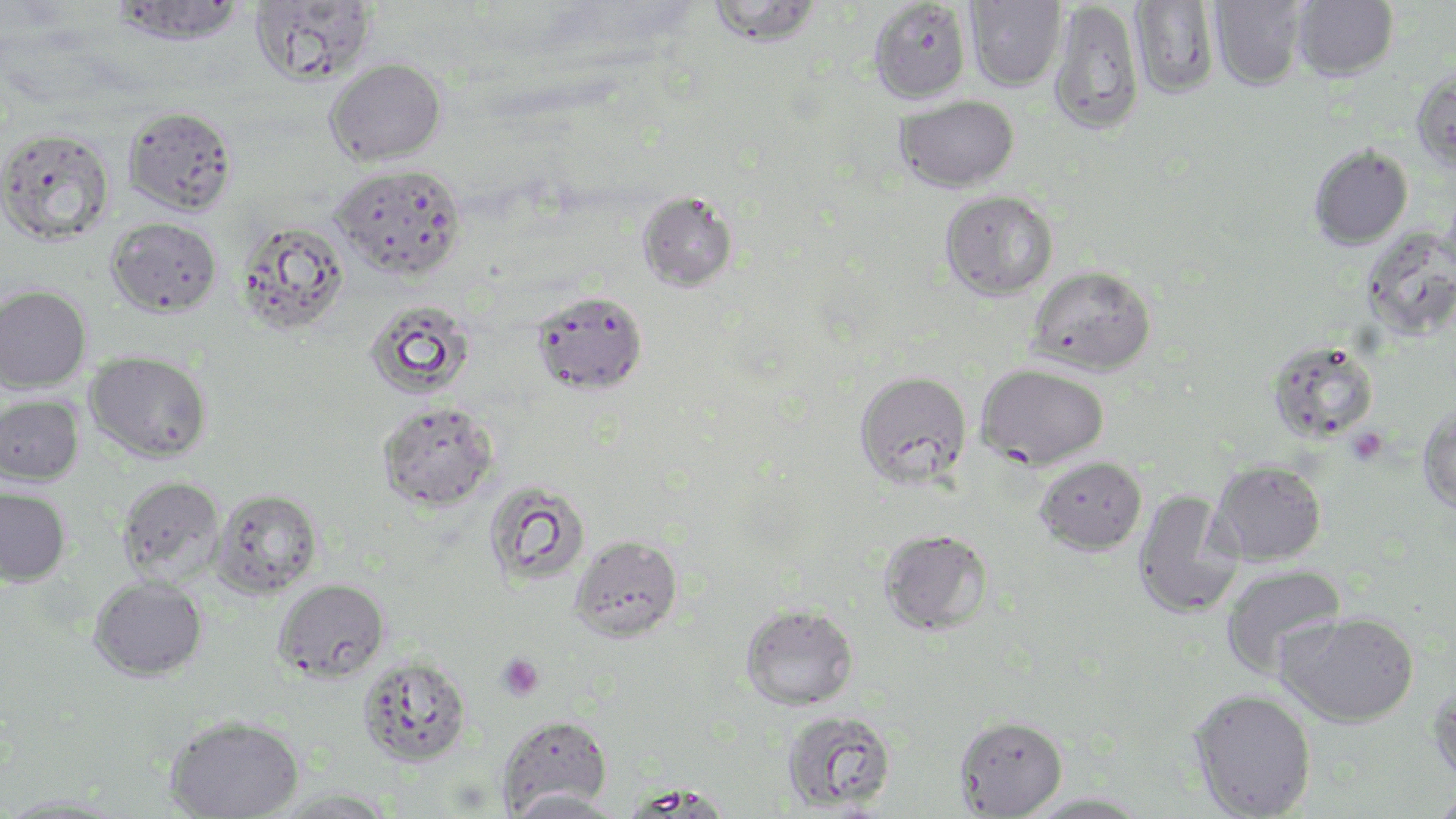

Summary:
  - Coordinate format: approximate bounding boxes as named x1/y1/x2/y2 corners in pixels
  - Platelet locations: (x1=1359, y1=432, x2=1385, y2=458), (x1=496, y1=652, x2=545, y2=701)
  - Uninfected red blood cell locations: (x1=110, y1=0, x2=247, y2=46), (x1=249, y1=0, x2=377, y2=86), (x1=704, y1=0, x2=825, y2=47), (x1=964, y1=0, x2=1067, y2=91), (x1=1293, y1=0, x2=1398, y2=81), (x1=868, y1=1, x2=971, y2=104), (x1=1129, y1=1, x2=1219, y2=99), (x1=1209, y1=1, x2=1307, y2=91), (x1=1048, y1=2, x2=1143, y2=135), (x1=326, y1=57, x2=446, y2=166), (x1=1411, y1=68, x2=1456, y2=173), (x1=895, y1=95, x2=1019, y2=193), (x1=121, y1=105, x2=237, y2=216), (x1=0, y1=128, x2=114, y2=245), (x1=1308, y1=144, x2=1413, y2=250), (x1=331, y1=164, x2=467, y2=280), (x1=637, y1=191, x2=738, y2=293), (x1=940, y1=191, x2=1058, y2=300), (x1=106, y1=217, x2=222, y2=318), (x1=238, y1=221, x2=350, y2=334), (x1=1027, y1=264, x2=1156, y2=376), (x1=0, y1=284, x2=92, y2=393), (x1=531, y1=291, x2=647, y2=395), (x1=363, y1=299, x2=476, y2=400), (x1=1266, y1=340, x2=1380, y2=443), (x1=85, y1=350, x2=213, y2=464), (x1=975, y1=363, x2=1110, y2=470), (x1=853, y1=370, x2=972, y2=489), (x1=0, y1=394, x2=84, y2=486), (x1=377, y1=401, x2=499, y2=512), (x1=1417, y1=403, x2=1456, y2=514), (x1=1035, y1=456, x2=1147, y2=555), (x1=1209, y1=460, x2=1328, y2=566), (x1=116, y1=475, x2=225, y2=586), (x1=483, y1=480, x2=590, y2=588), (x1=0, y1=487, x2=71, y2=586), (x1=210, y1=488, x2=324, y2=599), (x1=1132, y1=490, x2=1244, y2=620), (x1=879, y1=528, x2=993, y2=635), (x1=569, y1=535, x2=683, y2=642), (x1=1219, y1=564, x2=1347, y2=681), (x1=89, y1=576, x2=207, y2=682), (x1=274, y1=578, x2=390, y2=683), (x1=740, y1=602, x2=859, y2=710), (x1=1276, y1=611, x2=1420, y2=727), (x1=358, y1=655, x2=472, y2=767), (x1=1427, y1=678, x2=1456, y2=790), (x1=1188, y1=688, x2=1317, y2=818), (x1=780, y1=708, x2=898, y2=813), (x1=497, y1=714, x2=612, y2=814), (x1=164, y1=715, x2=304, y2=818), (x1=954, y1=715, x2=1067, y2=817), (x1=269, y1=788, x2=395, y2=818), (x1=1425, y1=788, x2=1456, y2=819), (x1=503, y1=789, x2=621, y2=818), (x1=1020, y1=792, x2=1154, y2=819), (x1=0, y1=793, x2=128, y2=818)
  - Slide-level diagnosis: Plasmodium falciparum
  - Stain: May-Grünwald-Giemsa
  - Image size: 1456×819 pixels
  - Magnification: 1000x
  - Modality: optical microscopy
  - Field of view: one of a larger specimen
  - Preparation: thin blood film